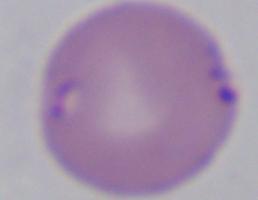

{
  "magnification": "1000x",
  "identification": "Babesia",
  "modality": "micrograph"
}